Classify this cell by malaria status.
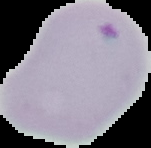
Parasitized.

Summary:
  - Image size: 151×148 pixels
  - Image type: segmented cell region on a black background
  - Preparation: thin blood smear